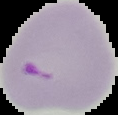

Summary:
  - Preparation: thin blood smear
  - Image size: 118×115 pixels
  - Image type: cell region segmented out of the field of view; surrounding area masked to black
  - Malaria status: parasitized